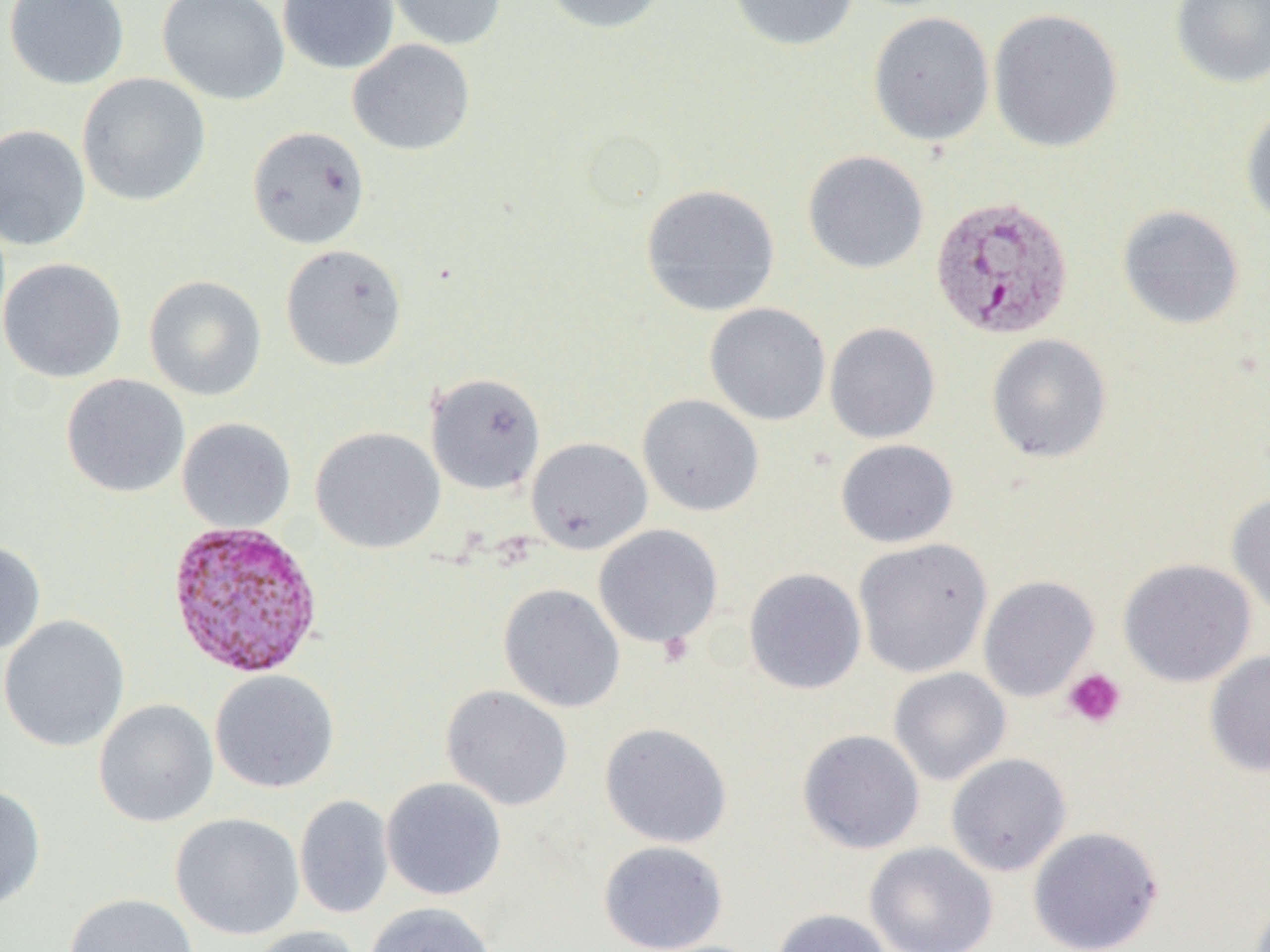 Approximate bounding boxes as (x1,y1)-(x2,y2) corner pairs in pixels. Platelet locations: (1063,668)-(1126,728). Uninfected red blood cell locations: (3,0)-(129,90), (157,0)-(290,105), (278,0)-(399,74), (386,0)-(507,50), (541,0)-(670,34), (726,0)-(859,52), (1170,0)-(1270,89), (987,7)-(1124,154), (868,11)-(995,146), (347,39)-(476,155), (76,73)-(211,207), (1240,105)-(1270,229), (0,124)-(91,250), (246,125)-(370,249), (802,150)-(929,274), (640,183)-(781,317), (1117,204)-(1245,330), (280,244)-(407,371), (0,257)-(126,382), (144,275)-(267,401), (704,303)-(831,426), (824,322)-(940,443), (987,334)-(1112,463), (425,372)-(546,495), (61,373)-(190,498), (637,394)-(764,517), (177,417)-(296,533), (310,426)-(445,554), (526,437)-(652,554), (836,439)-(958,548), (1227,491)-(1270,617), (593,524)-(724,649), (853,538)-(993,678), (0,540)-(46,654), (1117,558)-(1256,687), (743,567)-(867,695), (978,575)-(1099,702), (498,583)-(625,713), (0,615)-(130,753), (1204,650)-(1270,776), (888,667)-(1011,785), (210,669)-(340,793), (440,685)-(573,812), (93,699)-(219,827), (599,722)-(733,848), (797,729)-(925,854), (946,753)-(1072,876), (381,777)-(507,901), (0,783)-(46,909), (294,795)-(394,919), (170,813)-(305,940), (1028,826)-(1164,951), (598,840)-(728,951), (865,841)-(998,952), (64,892)-(199,952), (363,901)-(498,952), (772,908)-(894,952), (247,925)-(363,952). Plasmodium vivax-infected red blood cell locations: (932,194)-(1078,341), (172,520)-(331,679). Slide-level diagnosis: Plasmodium vivax. Light microscopy. Single field of view. Thin blood film. 1000x magnification. Image is 1270×952 pixels.